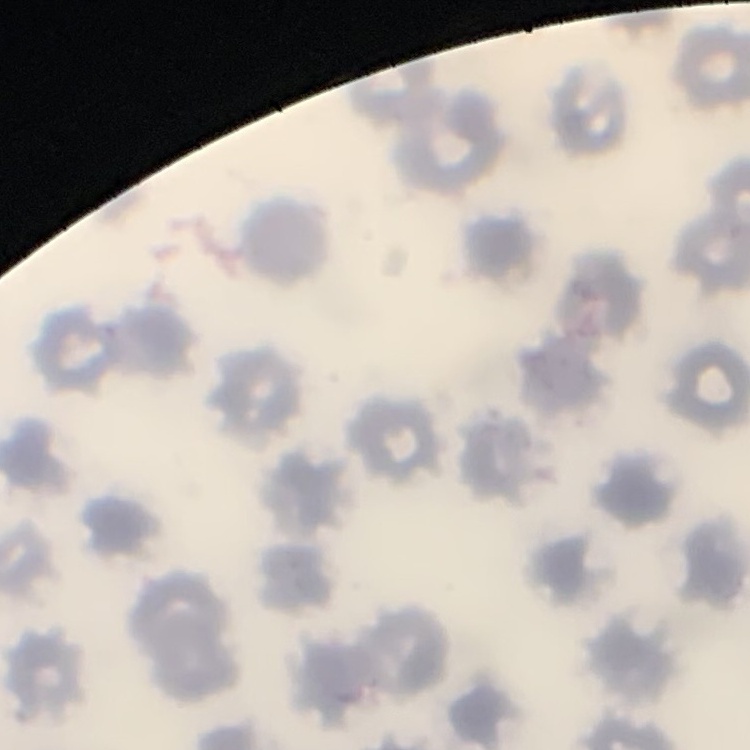

The red blood cells show no rouleaux formation. Square crop of a larger photomicrograph. Thin peripheral smear. Stained with either Field's or Giemsa.